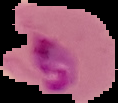
Summary:
  - Image size: 118×103 pixels
  - Image type: segmented cell region on a black background
  - Preparation: thin blood film
  - Result: Plasmodium parasites identified